Point out each Plasmodium parasite.
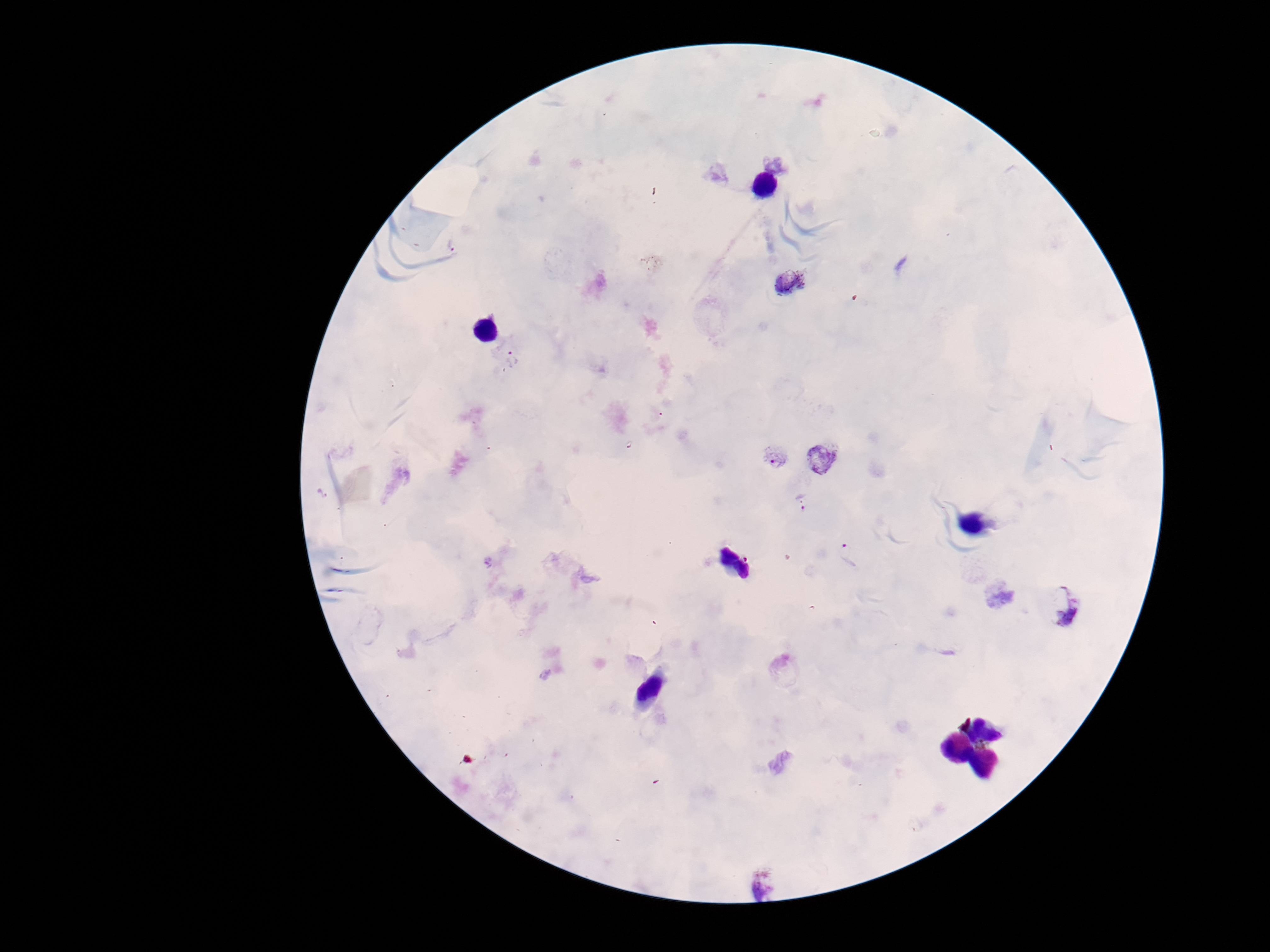
Approximate centers as [x, y] in pixels.
Plasmodium parasites: [777, 162], [789, 283], [512, 360], [774, 457], [820, 458], [803, 504], [850, 554], [1062, 604], [761, 886].

magnification = 100x
patient malaria status = infected
stain = Giemsa
field of view = one from this slide
image size = 1270×952 pixels
preparation = thick blood film
capture = smartphone camera through the microscope eyepiece